Assess this cell for malaria.
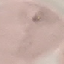
It is uninfected.

image type = cell patch, automatically extracted from a larger field of view and resized to 64 × 64 pixels
preparation = thin blood film
capture = smartphone camera at the microscope eyepiece
stain = Giemsa